Name the parasite shown.
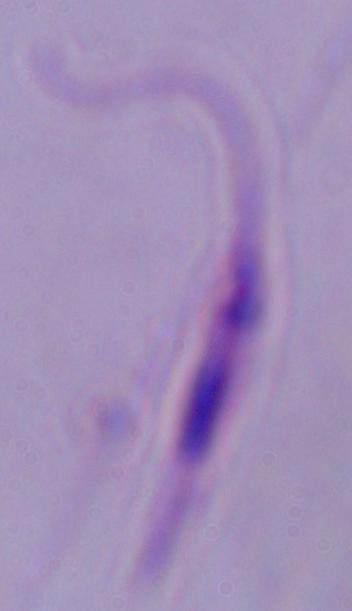
Leishmania.

Micrograph. 1000x magnification.